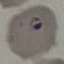
Summary:
  - Result: malaria parasites identified
  - Preparation: thin smear
  - Image type: automatically extracted cell patch, resized to 64 × 64 pixels
  - Capture: smartphone camera at the microscope eyepiece
  - Stain: Giemsa